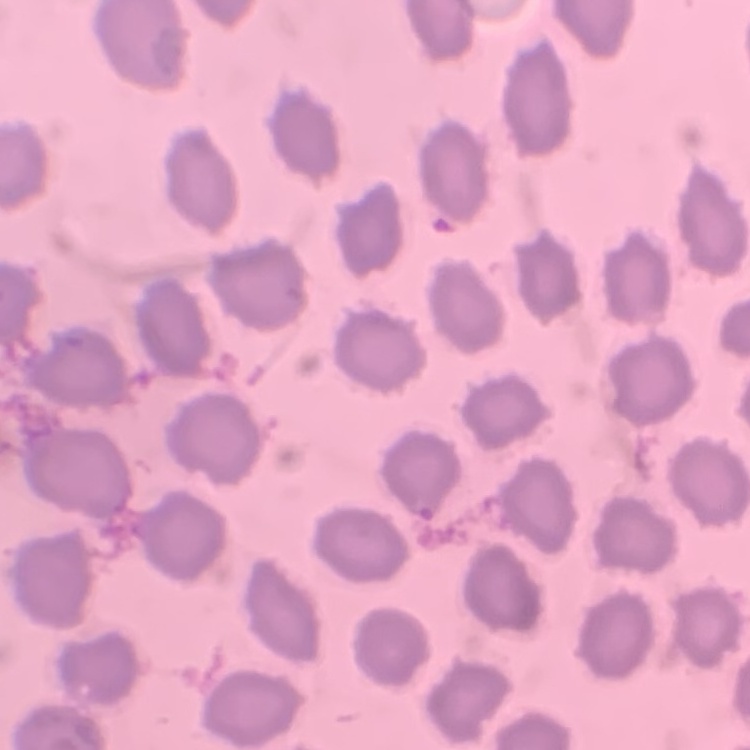
erythrocyte morphology = no rouleaux formation
preparation = thin peripheral smear
stain = Field's or Giemsa
image type = one tile cut from a larger photomicrograph